Report the malaria status of this cell.
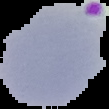

It is parasitized.

Summary:
  - Image size: 109×109 pixels
  - Preparation: thin blood film
  - Image type: segmented cell region with the area outside set to black